Give the extent of all Plasmodium falciparum-infected red blood cells.
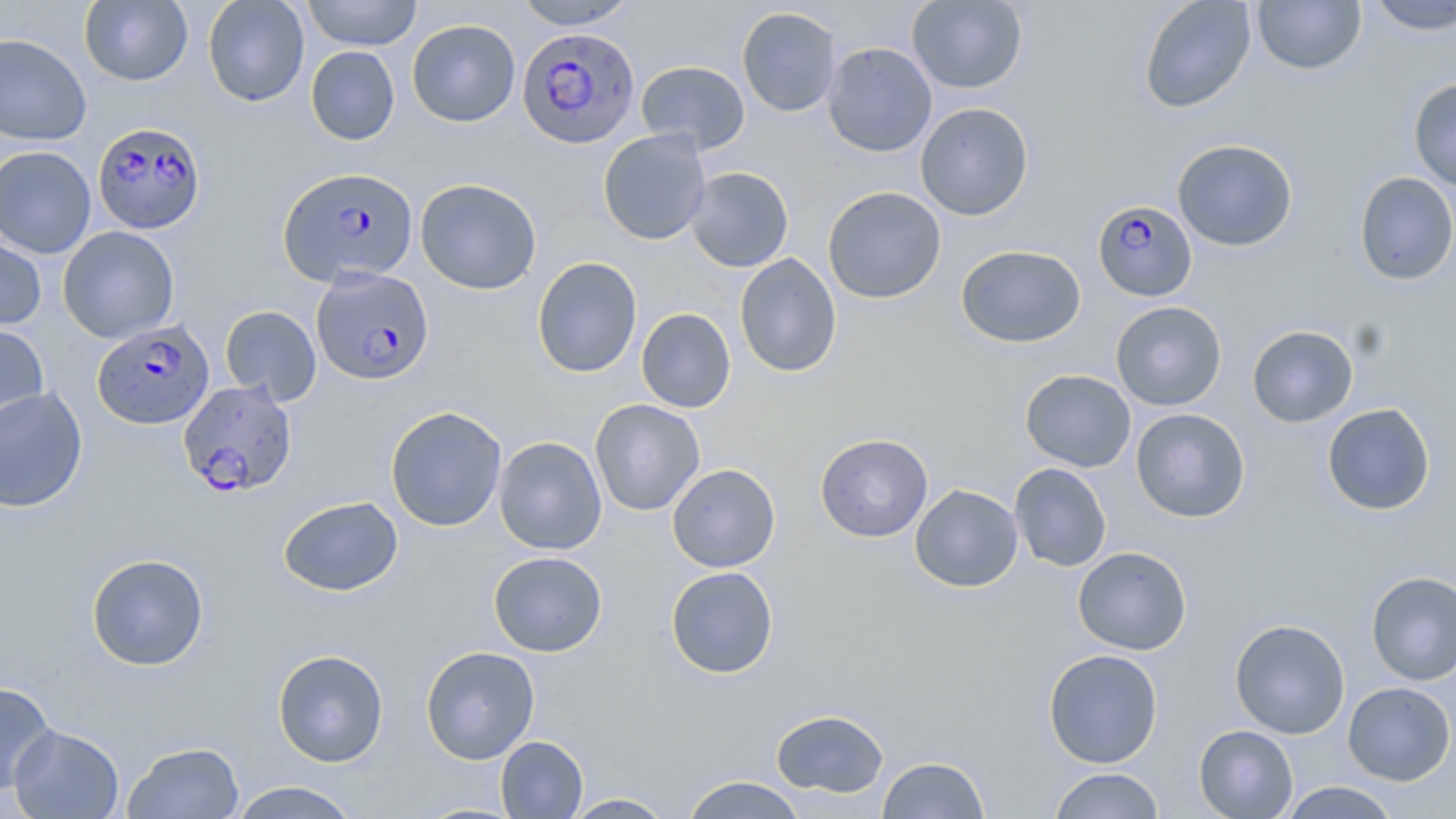
Approximate bounding boxes as [x1, y1, x2, y2] in pixels.
Plasmodium falciparum-infected red blood cells: [518, 26, 640, 148], [93, 121, 206, 234], [279, 167, 418, 287], [1092, 200, 1198, 302], [311, 268, 434, 385], [93, 320, 214, 430], [177, 380, 296, 498].

slide-level diagnosis = Plasmodium falciparum
image size = 1456×819 pixels
magnification = 1000x
modality = light microscopy
stain = May-Grünwald-Giemsa
uninfected red blood cell locations = approximate bounding boxes as [x1, y1, x2, y2] in pixels: [202, 0, 310, 107], [301, 0, 422, 50], [513, 0, 640, 30], [907, 0, 1028, 94], [1138, 0, 1256, 113], [79, 1, 193, 86], [1251, 1, 1367, 75], [1364, 1, 1456, 35], [736, 7, 842, 117], [407, 19, 521, 127], [0, 33, 92, 146], [822, 42, 938, 157], [305, 46, 400, 145], [636, 60, 750, 155], [1408, 77, 1456, 192], [915, 102, 1034, 221], [598, 129, 711, 245], [1172, 139, 1298, 251], [0, 145, 97, 259], [685, 167, 794, 272], [1353, 172, 1456, 285], [415, 178, 542, 295], [822, 186, 946, 304], [57, 226, 180, 343], [0, 234, 47, 331], [956, 245, 1086, 348], [734, 253, 842, 378], [532, 256, 642, 378], [1110, 301, 1227, 410], [219, 305, 321, 405], [636, 308, 736, 413], [0, 320, 49, 435], [1246, 324, 1359, 428], [1020, 369, 1137, 472], [0, 386, 88, 513], [589, 398, 705, 516], [1321, 403, 1436, 516], [385, 405, 507, 532], [1130, 408, 1250, 522], [815, 433, 933, 542], [494, 436, 607, 555], [667, 463, 781, 572], [1009, 463, 1112, 572], [909, 484, 1023, 592], [278, 496, 403, 597], [1072, 546, 1192, 655], [488, 551, 607, 657], [86, 553, 209, 671], [665, 566, 779, 679], [1366, 571, 1456, 686], [1229, 618, 1350, 739], [420, 645, 540, 764], [272, 648, 389, 767], [1043, 649, 1163, 768], [0, 681, 56, 795], [1342, 681, 1455, 785], [770, 709, 890, 797], [9, 724, 124, 818], [1194, 724, 1298, 819], [495, 736, 588, 818], [123, 741, 245, 819], [877, 756, 990, 818], [1048, 768, 1165, 818], [680, 775, 809, 818], [227, 781, 362, 819], [1278, 781, 1403, 818], [561, 792, 677, 818]
field of view = one of a larger specimen
preparation = thin blood film